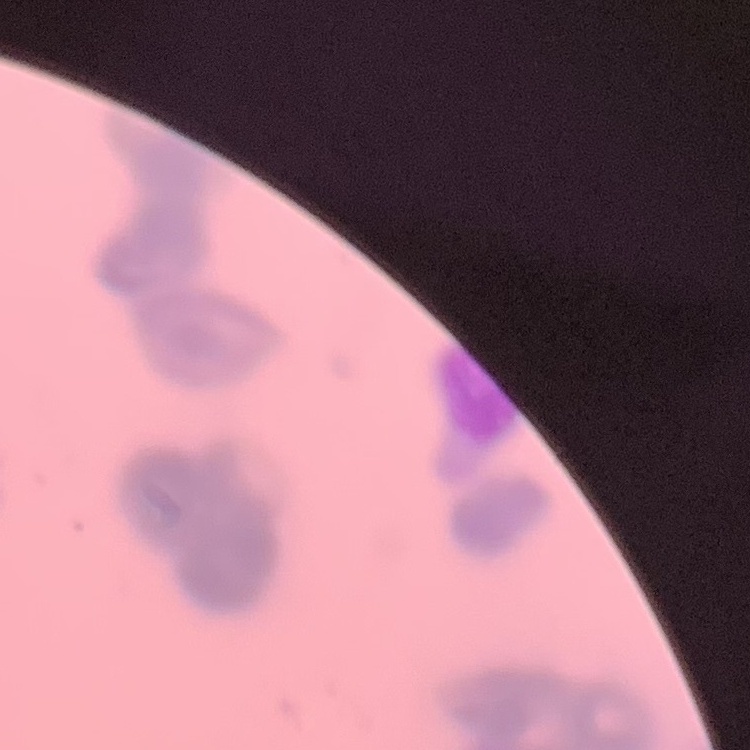

erythrocyte_morphology: rouleaux formation
preparation: thin blood smear
image_type: square crop of a larger photomicrograph
stain: Field's or Giemsa